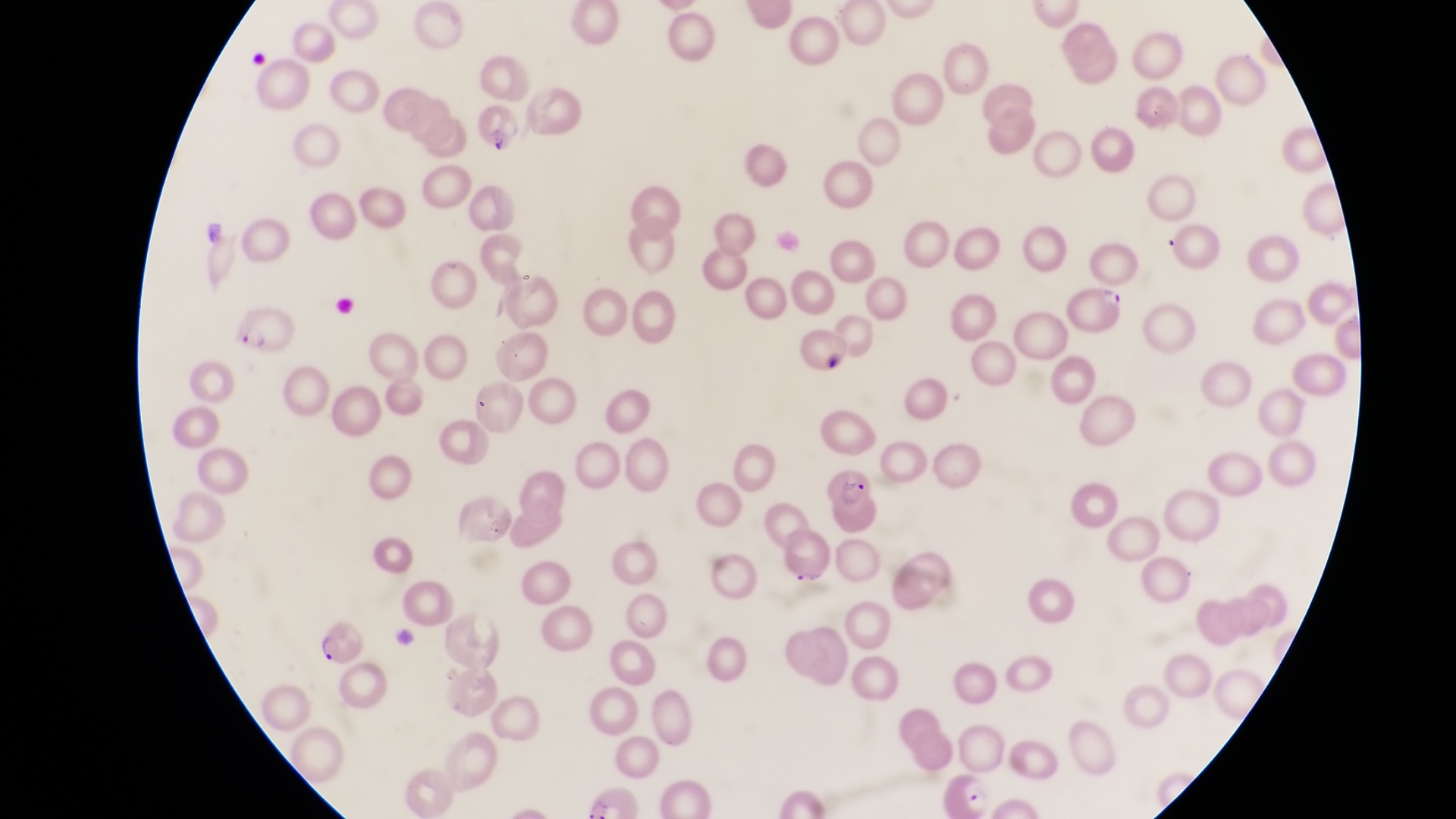

parasitised_red_blood_cell_locations: 'approximate bounding boxes as {left, top, right, bottom} in pixels: {1067, 278, 1125, 331}, {237, 304, 296, 357}, {825, 465, 878, 537}, {312, 626, 365, 665}'
country: Uganda
field_of_view: single
preparation: thin blood smear
magnification: 1000x
capture: smartphone photograph through the eyepiece of an Olympus CX-23 microscope
image_size: 1456×819 pixels
artifact_platelet_like_body_stain_precipitate_or_debris_locations: 'approximate bounding boxes as {left, top, right, bottom} in pixels: {482, 121, 506, 160}'